Report the malaria status of this cell.
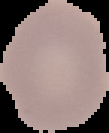

It is parasitized.

image size = 109×133 pixels
preparation = thin blood smear
image type = segmented cell region with the area outside set to black